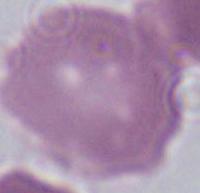
Summary:
  - Identification: red blood cell
  - Modality: micrograph
  - Magnification: 1000x